Assess this cell for malaria.
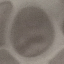

Uninfected.

Photographed with a smartphone camera at the microscope eyepiece. Automatically extracted cell patch, resized to 64 × 64 pixels. Thin smear of blood. Giemsa-stained preparation.